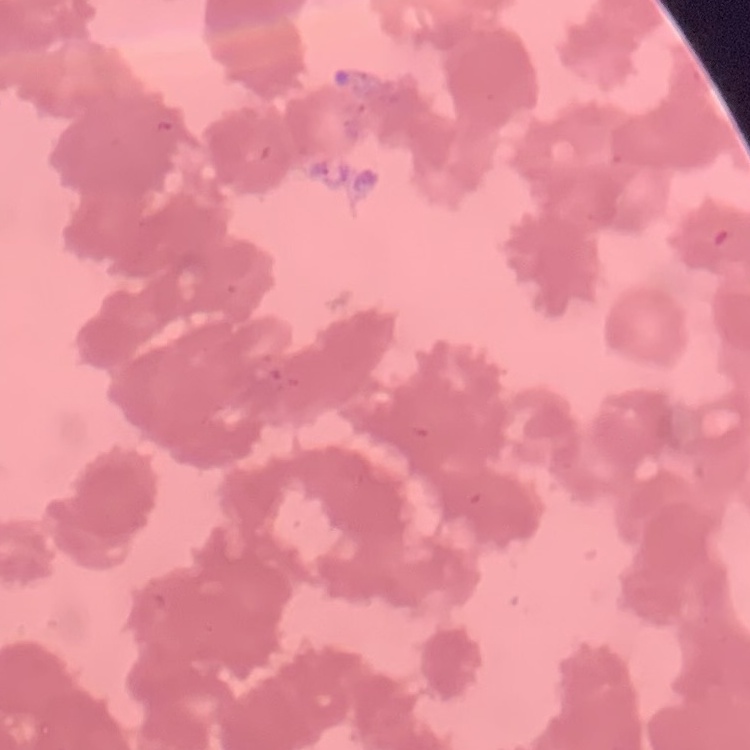

erythrocyte_morphology: rouleaux formation
stain: Field's or Giemsa
preparation: thin blood smear
image_type: square crop of a larger photomicrograph